Identify the parasite.
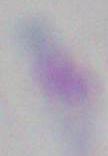

Toxoplasma gondii.

modality: micrograph
magnification: 1000x